Classify this cell by malaria status.
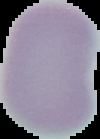
Uninfected.

image type = segmented cell region on a black background
image size = 100×139 pixels
preparation = thin blood smear